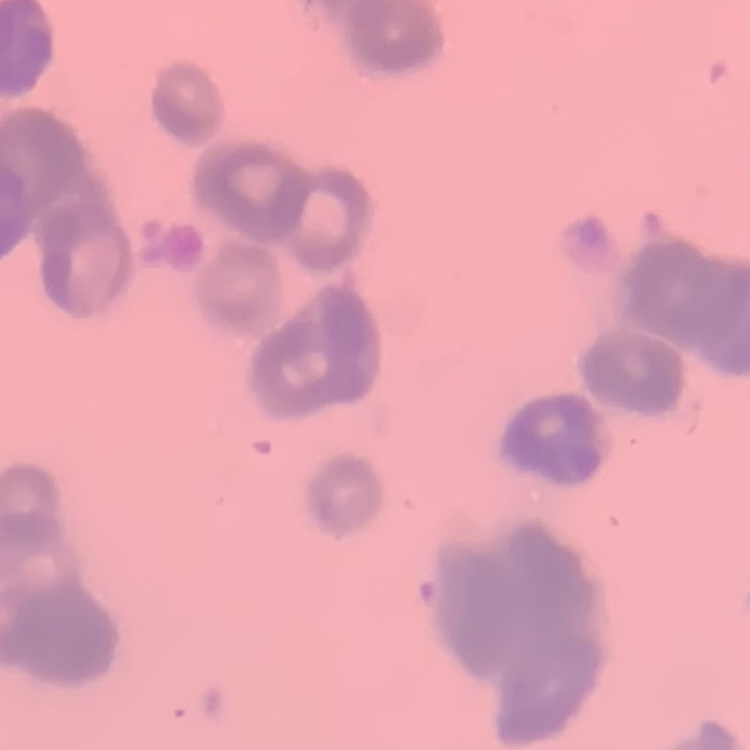
Summary:
  - Erythrocyte morphology: rouleaux formation
  - Preparation: thin peripheral smear
  - Stain: Field's or Giemsa
  - Image type: one tile cut from a larger photomicrograph